Locate and identify every blood parasite.
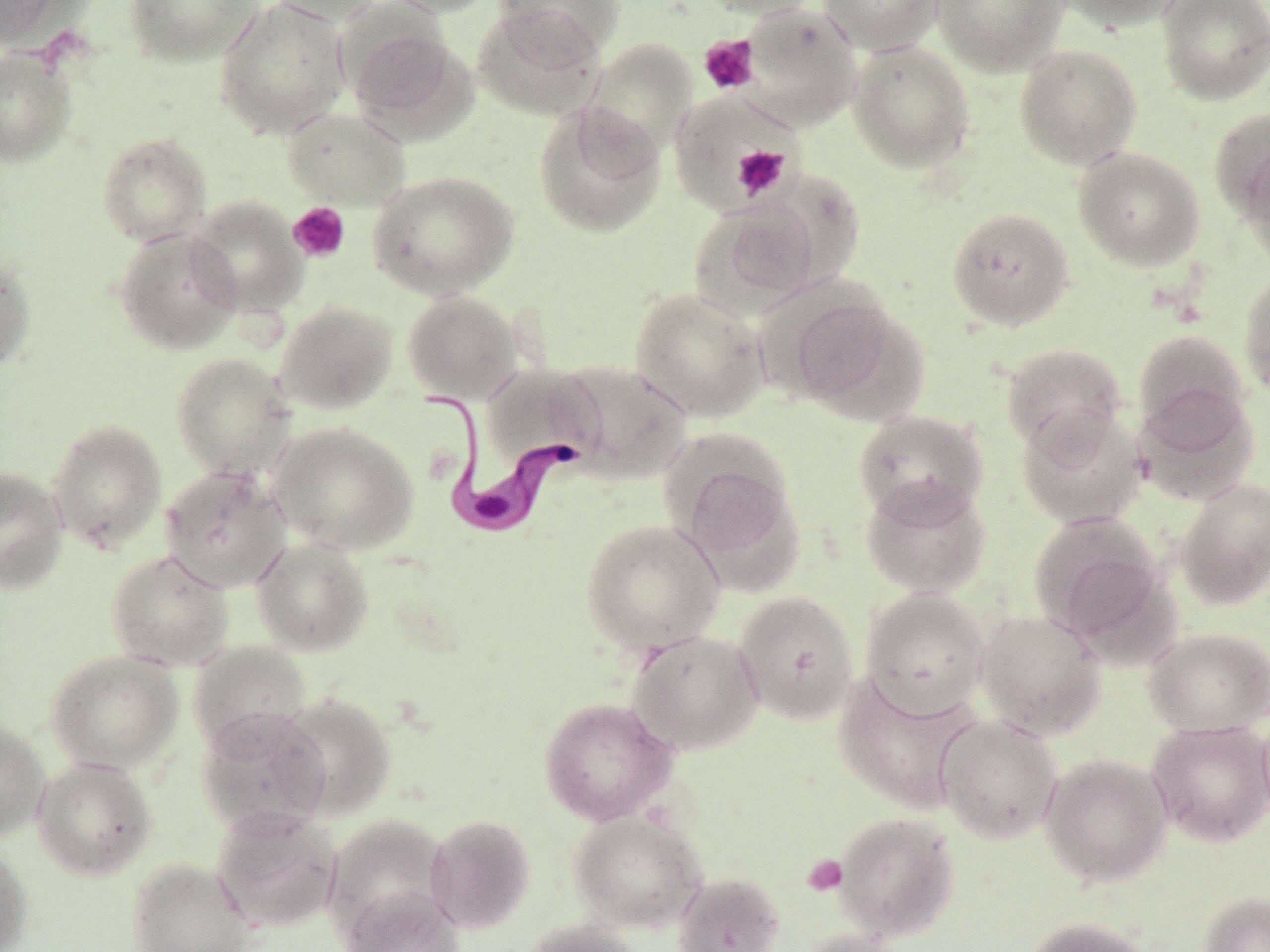

Approximate bounding boxes as named x1/y1/x2/y2 corners in pixels.
Trypanosoma brucei: (x1=417, y1=386, x2=575, y2=539).
No Plasmodium falciparum, Plasmodium ovale, Plasmodium malariae, Plasmodium vivax, or Babesia divergens observed.

slide-level diagnosis = Trypanosoma brucei
platelet locations = approximate bounding boxes as named x1/y1/x2/y2 corners in pixels: (x1=699, y1=34, x2=759, y2=95), (x1=732, y1=144, x2=790, y2=200), (x1=288, y1=202, x2=350, y2=262), (x1=803, y1=854, x2=848, y2=895)
preparation = thin blood film
image size = 1270×952 pixels
stain = May-Grünwald-Giemsa
magnification = 1000x
uninfected red blood cell locations = approximate bounding boxes as named x1/y1/x2/y2 corners in pixels: (x1=0, y1=0, x2=62, y2=47), (x1=121, y1=0, x2=263, y2=67), (x1=214, y1=0, x2=351, y2=139), (x1=262, y1=0, x2=387, y2=25), (x1=380, y1=0, x2=504, y2=17), (x1=493, y1=0, x2=624, y2=60), (x1=695, y1=0, x2=821, y2=19), (x1=818, y1=0, x2=945, y2=55), (x1=931, y1=0, x2=1070, y2=75), (x1=1052, y1=0, x2=1188, y2=32), (x1=1157, y1=0, x2=1270, y2=105), (x1=471, y1=4, x2=607, y2=118), (x1=738, y1=4, x2=864, y2=129), (x1=344, y1=22, x2=476, y2=140), (x1=582, y1=39, x2=698, y2=158), (x1=847, y1=39, x2=976, y2=174), (x1=1013, y1=43, x2=1143, y2=170), (x1=0, y1=48, x2=77, y2=167), (x1=668, y1=92, x2=798, y2=209), (x1=533, y1=101, x2=667, y2=239), (x1=281, y1=106, x2=410, y2=210), (x1=1208, y1=107, x2=1270, y2=223), (x1=97, y1=132, x2=212, y2=246), (x1=1236, y1=139, x2=1270, y2=268), (x1=1072, y1=146, x2=1206, y2=271), (x1=368, y1=170, x2=520, y2=299), (x1=187, y1=195, x2=308, y2=316), (x1=689, y1=197, x2=822, y2=318), (x1=947, y1=206, x2=1075, y2=330), (x1=113, y1=227, x2=243, y2=355), (x1=0, y1=251, x2=36, y2=374), (x1=1239, y1=272, x2=1270, y2=398), (x1=628, y1=287, x2=770, y2=422), (x1=401, y1=290, x2=522, y2=403), (x1=781, y1=290, x2=925, y2=423), (x1=275, y1=300, x2=398, y2=414), (x1=1132, y1=327, x2=1251, y2=436), (x1=1000, y1=342, x2=1127, y2=457), (x1=170, y1=351, x2=296, y2=481), (x1=479, y1=362, x2=605, y2=477), (x1=555, y1=362, x2=691, y2=484), (x1=1133, y1=384, x2=1260, y2=505), (x1=1016, y1=405, x2=1148, y2=530), (x1=852, y1=408, x2=989, y2=525), (x1=47, y1=420, x2=167, y2=553), (x1=267, y1=421, x2=419, y2=556), (x1=669, y1=443, x2=803, y2=583), (x1=160, y1=464, x2=292, y2=592), (x1=0, y1=465, x2=69, y2=593), (x1=860, y1=476, x2=991, y2=598), (x1=1174, y1=477, x2=1270, y2=610), (x1=1027, y1=510, x2=1166, y2=642), (x1=581, y1=519, x2=725, y2=653), (x1=250, y1=536, x2=375, y2=656), (x1=106, y1=549, x2=234, y2=670), (x1=860, y1=588, x2=990, y2=718), (x1=733, y1=590, x2=860, y2=726), (x1=974, y1=609, x2=1108, y2=740), (x1=1143, y1=626, x2=1270, y2=737), (x1=626, y1=629, x2=764, y2=755), (x1=188, y1=640, x2=311, y2=756), (x1=44, y1=649, x2=184, y2=774), (x1=832, y1=671, x2=982, y2=814), (x1=273, y1=692, x2=397, y2=820), (x1=537, y1=696, x2=676, y2=826), (x1=195, y1=707, x2=332, y2=838), (x1=1255, y1=711, x2=1270, y2=828), (x1=935, y1=713, x2=1063, y2=844), (x1=0, y1=718, x2=51, y2=842), (x1=1146, y1=719, x2=1270, y2=847), (x1=1040, y1=752, x2=1173, y2=887), (x1=31, y1=756, x2=158, y2=881), (x1=211, y1=806, x2=343, y2=933), (x1=568, y1=810, x2=708, y2=933), (x1=832, y1=811, x2=961, y2=942), (x1=425, y1=814, x2=536, y2=934), (x1=323, y1=816, x2=453, y2=941), (x1=0, y1=841, x2=34, y2=952), (x1=126, y1=856, x2=257, y2=952), (x1=672, y1=870, x2=785, y2=952), (x1=340, y1=887, x2=466, y2=952), (x1=1196, y1=891, x2=1270, y2=952), (x1=1024, y1=916, x2=1158, y2=952), (x1=521, y1=918, x2=641, y2=952), (x1=799, y1=929, x2=917, y2=952)
modality = light microscopy
field of view = one of a larger specimen